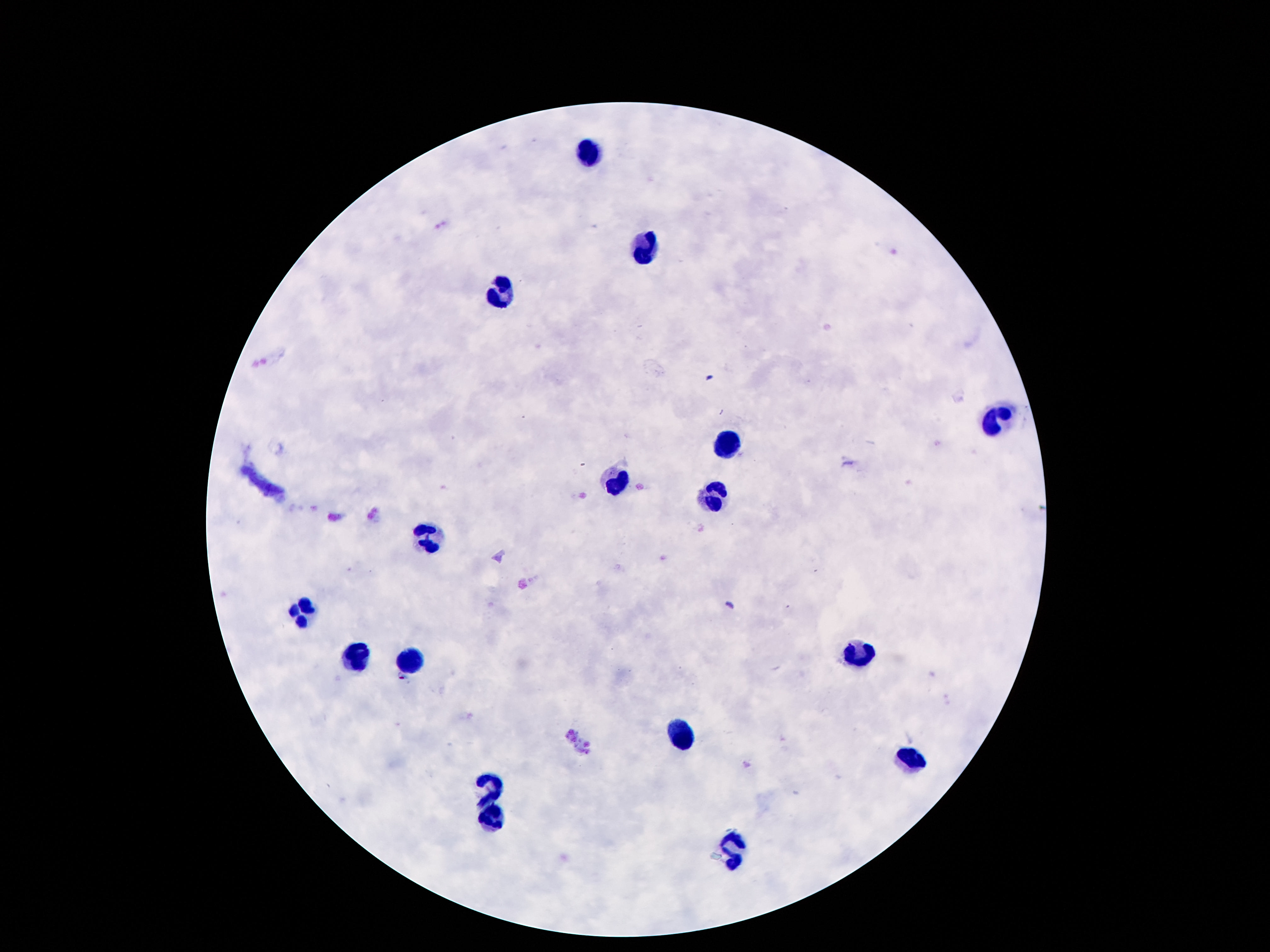

capture = smartphone camera through the microscope eyepiece
stain = Giemsa
leukocyte locations = approximate object centers, in pixels from the top-left corner: (x=587, y=155), (x=644, y=249), (x=505, y=294), (x=993, y=424), (x=726, y=443), (x=614, y=484), (x=718, y=494), (x=421, y=535), (x=302, y=607), (x=866, y=650), (x=356, y=656), (x=411, y=661), (x=681, y=736), (x=911, y=762), (x=489, y=791), (x=491, y=818), (x=735, y=859)
magnification = 100x
preparation = thick blood smear
image size = 1270×952 pixels
patient malaria status = uninfected
field of view = single